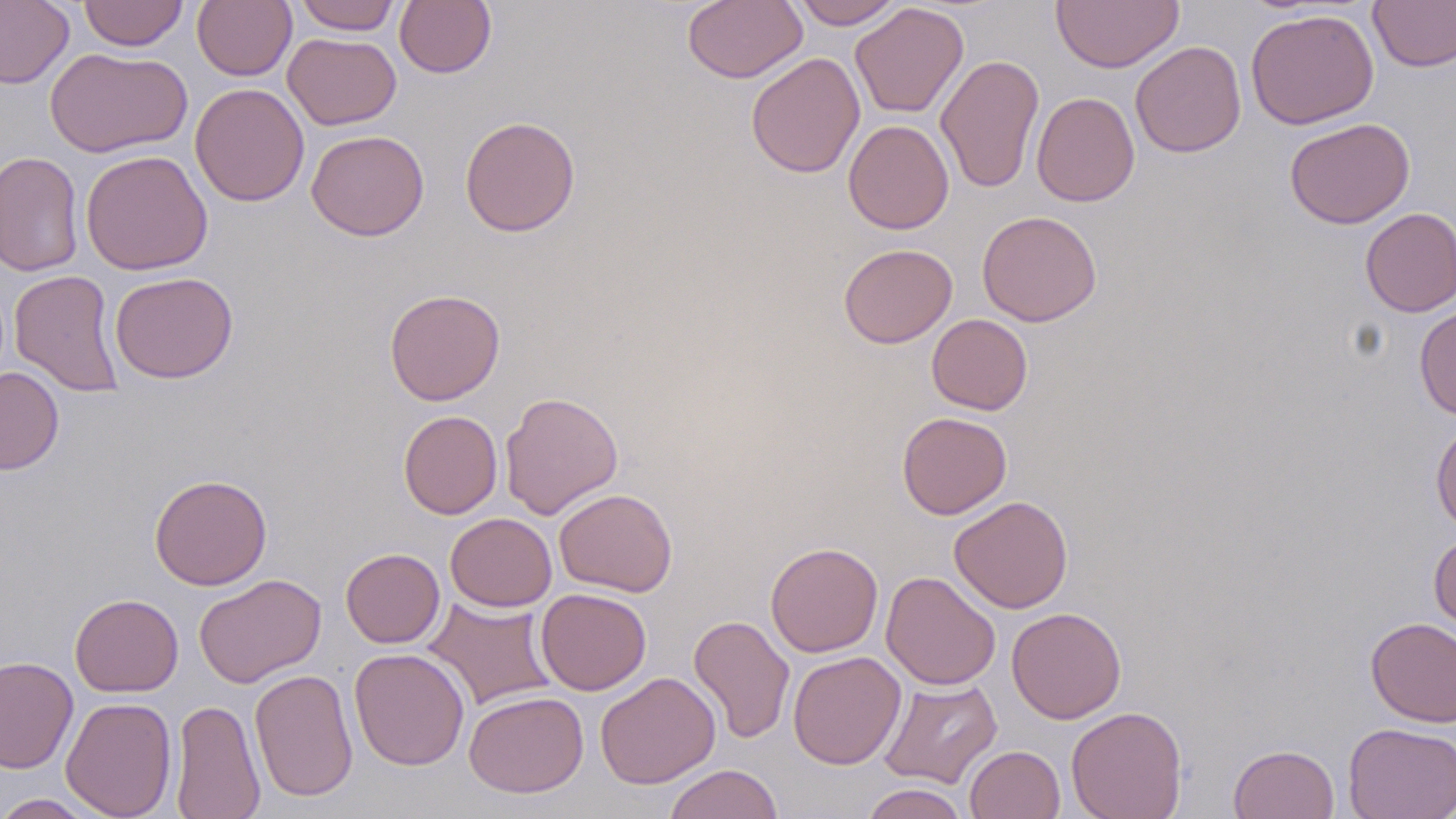

Approximate bounding boxes as named x1/y1/x2/y2 corners in pixels. Uninfected red blood cell locations: (x1=78, y1=0, x2=189, y2=51), (x1=193, y1=0, x2=296, y2=81), (x1=293, y1=0, x2=402, y2=34), (x1=394, y1=0, x2=496, y2=78), (x1=791, y1=0, x2=903, y2=29), (x1=1367, y1=0, x2=1456, y2=72), (x1=0, y1=1, x2=73, y2=89), (x1=682, y1=1, x2=807, y2=84), (x1=1051, y1=1, x2=1184, y2=73), (x1=850, y1=2, x2=969, y2=118), (x1=1245, y1=8, x2=1379, y2=130), (x1=283, y1=32, x2=401, y2=130), (x1=1131, y1=41, x2=1247, y2=158), (x1=45, y1=46, x2=192, y2=159), (x1=746, y1=52, x2=865, y2=179), (x1=935, y1=53, x2=1044, y2=194), (x1=190, y1=83, x2=309, y2=206), (x1=1031, y1=91, x2=1140, y2=207), (x1=459, y1=115, x2=580, y2=237), (x1=1284, y1=117, x2=1415, y2=228), (x1=843, y1=119, x2=955, y2=234), (x1=306, y1=129, x2=430, y2=241), (x1=81, y1=149, x2=213, y2=275), (x1=0, y1=150, x2=85, y2=277), (x1=1359, y1=208, x2=1456, y2=317), (x1=977, y1=210, x2=1102, y2=326), (x1=838, y1=243, x2=957, y2=349), (x1=8, y1=269, x2=125, y2=397), (x1=110, y1=271, x2=238, y2=384), (x1=384, y1=288, x2=505, y2=406), (x1=1414, y1=304, x2=1456, y2=419), (x1=926, y1=314, x2=1032, y2=415), (x1=0, y1=367, x2=64, y2=474), (x1=499, y1=390, x2=623, y2=519), (x1=398, y1=410, x2=502, y2=519), (x1=897, y1=411, x2=1012, y2=519), (x1=1430, y1=417, x2=1456, y2=533), (x1=149, y1=473, x2=273, y2=590), (x1=554, y1=489, x2=677, y2=597), (x1=949, y1=495, x2=1073, y2=613), (x1=445, y1=512, x2=557, y2=612), (x1=1429, y1=531, x2=1456, y2=636), (x1=765, y1=541, x2=883, y2=657), (x1=340, y1=548, x2=445, y2=648), (x1=881, y1=571, x2=1001, y2=690), (x1=194, y1=573, x2=326, y2=688), (x1=536, y1=588, x2=652, y2=695), (x1=69, y1=594, x2=184, y2=697), (x1=422, y1=597, x2=558, y2=710), (x1=1006, y1=607, x2=1126, y2=724), (x1=689, y1=614, x2=795, y2=744), (x1=1365, y1=617, x2=1456, y2=727), (x1=349, y1=648, x2=470, y2=771), (x1=787, y1=651, x2=906, y2=770), (x1=0, y1=656, x2=78, y2=773), (x1=249, y1=669, x2=359, y2=801), (x1=594, y1=671, x2=720, y2=789), (x1=878, y1=677, x2=1003, y2=789), (x1=464, y1=691, x2=589, y2=798), (x1=60, y1=696, x2=177, y2=818), (x1=170, y1=699, x2=265, y2=818), (x1=1066, y1=706, x2=1187, y2=819), (x1=1343, y1=722, x2=1456, y2=819), (x1=965, y1=744, x2=1065, y2=819), (x1=1228, y1=744, x2=1339, y2=819), (x1=663, y1=764, x2=784, y2=819), (x1=860, y1=783, x2=969, y2=819), (x1=0, y1=793, x2=103, y2=819). Slide-level diagnosis: negative for blood parasites. Captured at 1000x magnification. Image is 1456×819 pixels. Thin blood smear. Light microscopy. One field of a larger specimen. May-Grünwald-Giemsa-stained preparation.